Locate every Plasmodium parasite.
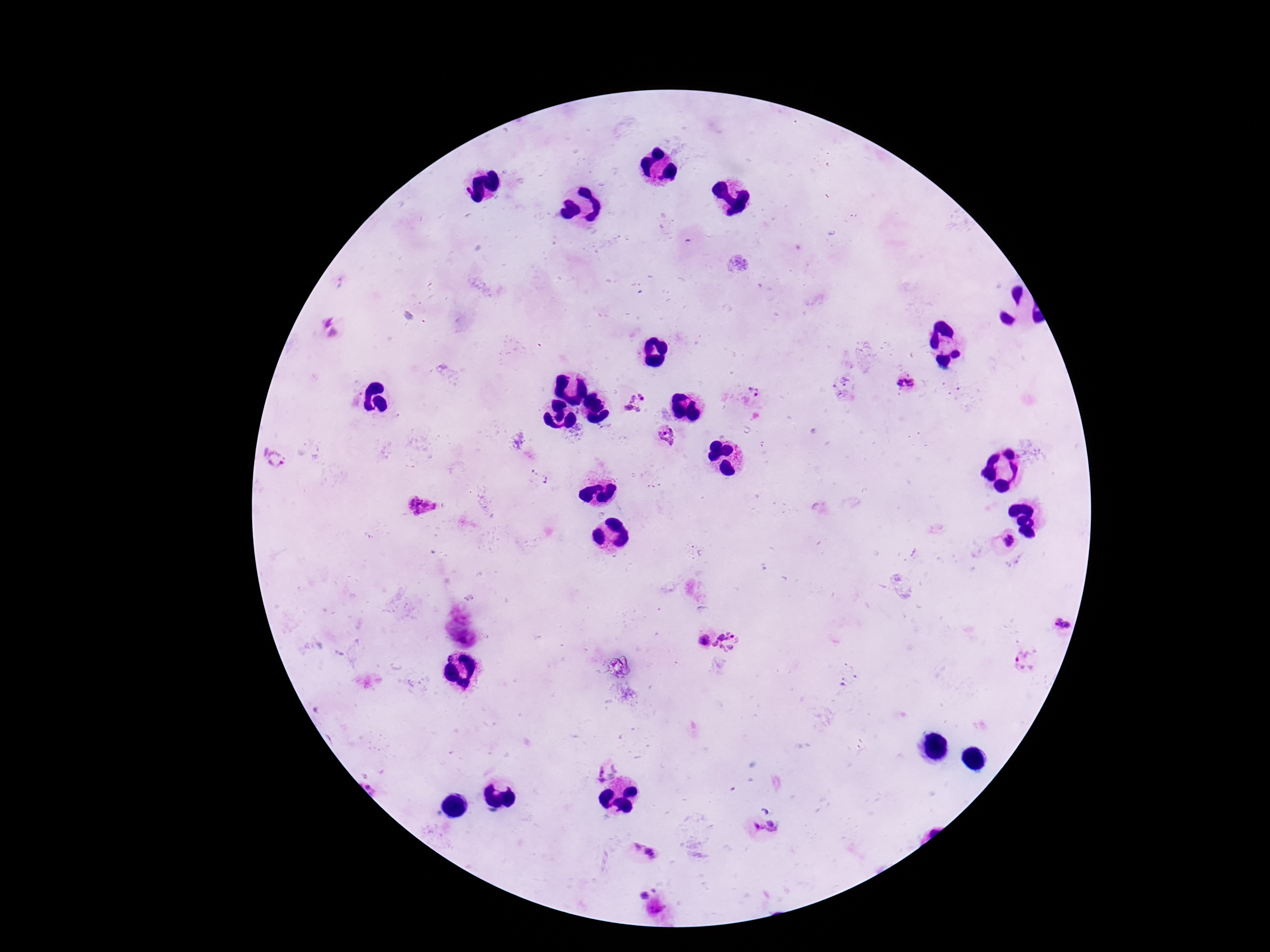
Approximate centers as {x, y} in pixels.
Plasmodium parasites: {846, 380}, {906, 385}, {834, 386}, {754, 391}, {842, 395}, {635, 403}, {578, 434}, {666, 436}, {519, 441}, {274, 459}, {423, 504}, {1010, 541}, {1064, 626}, {705, 641}, {729, 642}, {1026, 661}, {603, 768}, {757, 826}, {775, 826}, {642, 852}, {643, 889}, {658, 911}.

Summary:
  - Image size: 1270×952 pixels
  - Preparation: thick blood smear
  - Capture: smartphone camera through the microscope eyepiece
  - Magnification: 100x
  - Stain: Giemsa
  - Field of view: single
  - Patient malaria status: positive